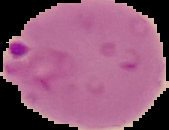

Summary:
  - Image size: 169×130 pixels
  - Image type: cell region segmented out of the field of view; surrounding area masked to black
  - Preparation: thin blood smear
  - Malaria status: parasitized